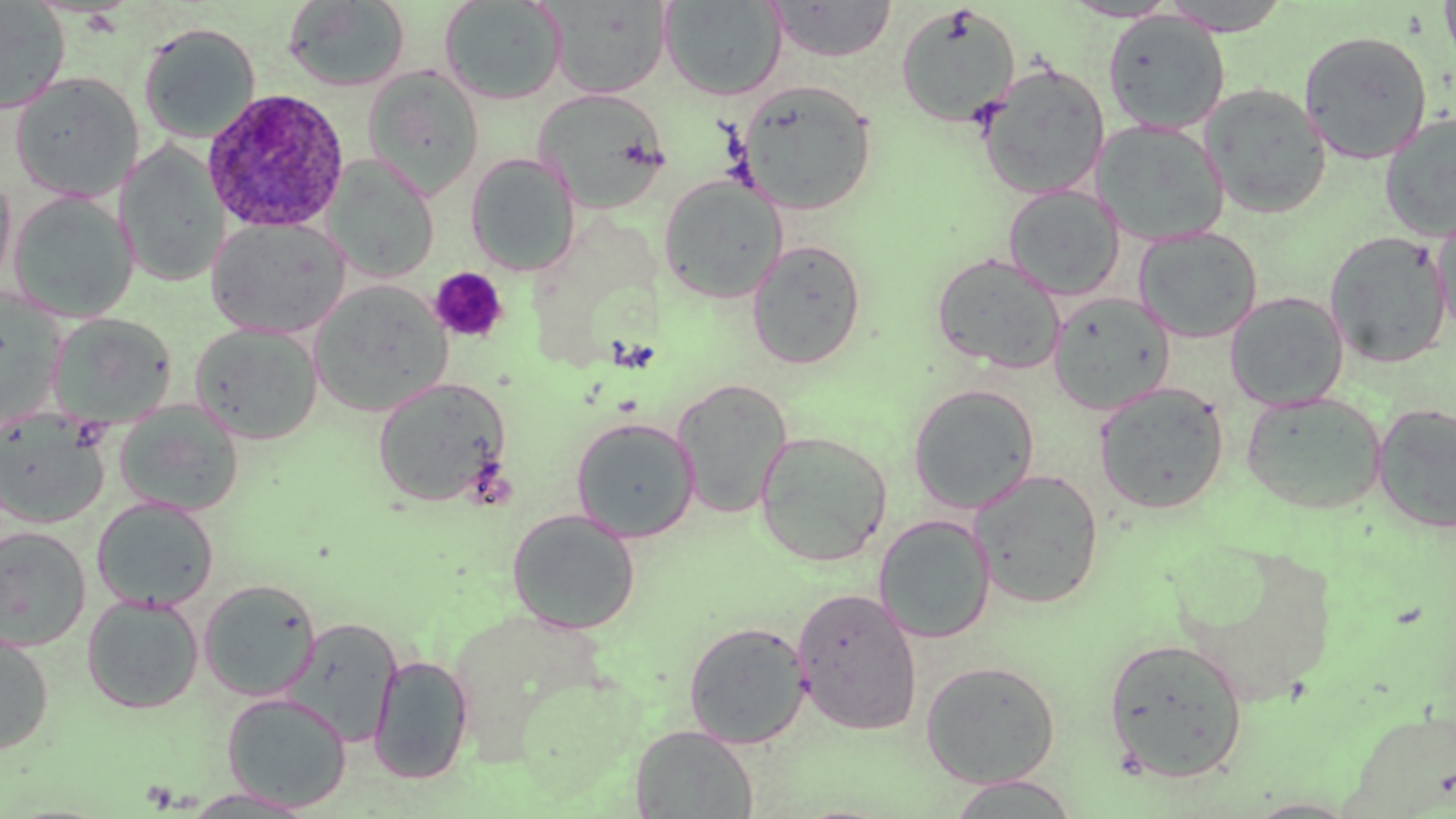
slide-level diagnosis = Plasmodium ovale
image size = 1456×819 pixels
Plasmodium ovale-infected red blood cell locations = approximate bounding boxes as named x1/y1/x2/y2 corners in pixels: (x1=202, y1=88, x2=350, y2=233)
preparation = thin blood smear
platelet locations = approximate bounding boxes as named x1/y1/x2/y2 corners in pixels: (x1=429, y1=267, x2=509, y2=344)
uninfected red blood cell locations = approximate bounding boxes as named x1/y1/x2/y2 corners in pixels: (x1=1060, y1=0, x2=1180, y2=22), (x1=1159, y1=0, x2=1291, y2=35), (x1=1439, y1=0, x2=1456, y2=72), (x1=0, y1=1, x2=71, y2=113), (x1=283, y1=1, x2=412, y2=93), (x1=439, y1=1, x2=567, y2=105), (x1=547, y1=1, x2=672, y2=99), (x1=659, y1=1, x2=786, y2=101), (x1=766, y1=1, x2=897, y2=61), (x1=895, y1=4, x2=1021, y2=128), (x1=1102, y1=11, x2=1231, y2=135), (x1=138, y1=22, x2=261, y2=144), (x1=1299, y1=29, x2=1433, y2=164), (x1=975, y1=61, x2=1111, y2=200), (x1=363, y1=66, x2=485, y2=198), (x1=10, y1=72, x2=143, y2=202), (x1=737, y1=80, x2=878, y2=215), (x1=1201, y1=83, x2=1332, y2=219), (x1=532, y1=89, x2=672, y2=212), (x1=1380, y1=113, x2=1456, y2=242), (x1=1091, y1=118, x2=1230, y2=246), (x1=117, y1=141, x2=229, y2=288), (x1=465, y1=153, x2=580, y2=276), (x1=324, y1=155, x2=439, y2=282), (x1=0, y1=169, x2=17, y2=293), (x1=657, y1=175, x2=789, y2=304), (x1=1003, y1=184, x2=1126, y2=300), (x1=9, y1=190, x2=139, y2=322), (x1=1431, y1=209, x2=1456, y2=341), (x1=205, y1=216, x2=352, y2=338), (x1=1133, y1=227, x2=1263, y2=342), (x1=1324, y1=231, x2=1452, y2=368), (x1=746, y1=239, x2=867, y2=370), (x1=931, y1=252, x2=1066, y2=374), (x1=309, y1=279, x2=454, y2=416), (x1=0, y1=289, x2=66, y2=429), (x1=1225, y1=291, x2=1349, y2=410), (x1=1047, y1=292, x2=1176, y2=415), (x1=47, y1=312, x2=178, y2=429), (x1=190, y1=322, x2=324, y2=445), (x1=373, y1=377, x2=512, y2=508), (x1=671, y1=377, x2=793, y2=519), (x1=1094, y1=382, x2=1230, y2=514), (x1=907, y1=383, x2=1040, y2=514), (x1=1240, y1=391, x2=1387, y2=515), (x1=114, y1=399, x2=245, y2=517), (x1=1372, y1=402, x2=1456, y2=535), (x1=0, y1=409, x2=110, y2=529), (x1=571, y1=417, x2=700, y2=541), (x1=754, y1=430, x2=892, y2=568), (x1=969, y1=469, x2=1105, y2=610), (x1=92, y1=497, x2=219, y2=611), (x1=506, y1=509, x2=641, y2=635), (x1=873, y1=514, x2=996, y2=644), (x1=0, y1=526, x2=92, y2=651), (x1=198, y1=579, x2=321, y2=701), (x1=791, y1=587, x2=923, y2=736), (x1=81, y1=594, x2=204, y2=713), (x1=282, y1=617, x2=403, y2=747), (x1=683, y1=621, x2=812, y2=748), (x1=0, y1=628, x2=55, y2=755), (x1=1102, y1=636, x2=1249, y2=784), (x1=369, y1=654, x2=474, y2=784), (x1=920, y1=660, x2=1061, y2=788), (x1=221, y1=692, x2=352, y2=812), (x1=1344, y1=708, x2=1456, y2=817), (x1=629, y1=725, x2=758, y2=817), (x1=943, y1=774, x2=1082, y2=818), (x1=178, y1=788, x2=318, y2=817)
magnification = 1000x
field of view = single
stain = May-Grünwald-Giemsa
modality = optical microscopy